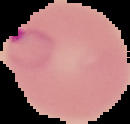
Summary:
  - Preparation: thin blood film
  - Image size: 130×124 pixels
  - Result: Plasmodium parasites detected
  - Image type: segmented cell region with the area outside set to black